Describe the morphology of the erythrocytes.
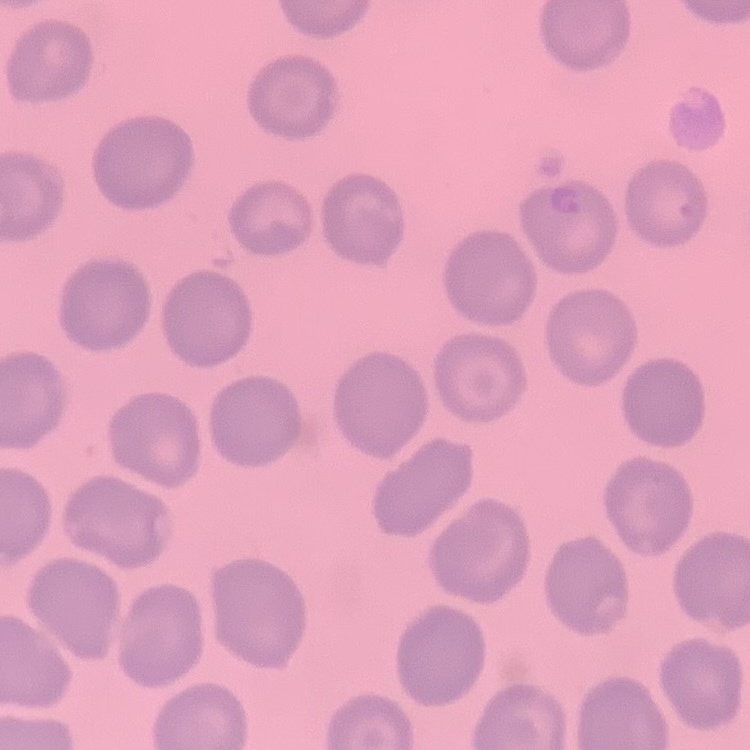
No rouleaux formation.

image type = square crop of a larger photomicrograph
stain = Field's or Giemsa
preparation = thin blood film